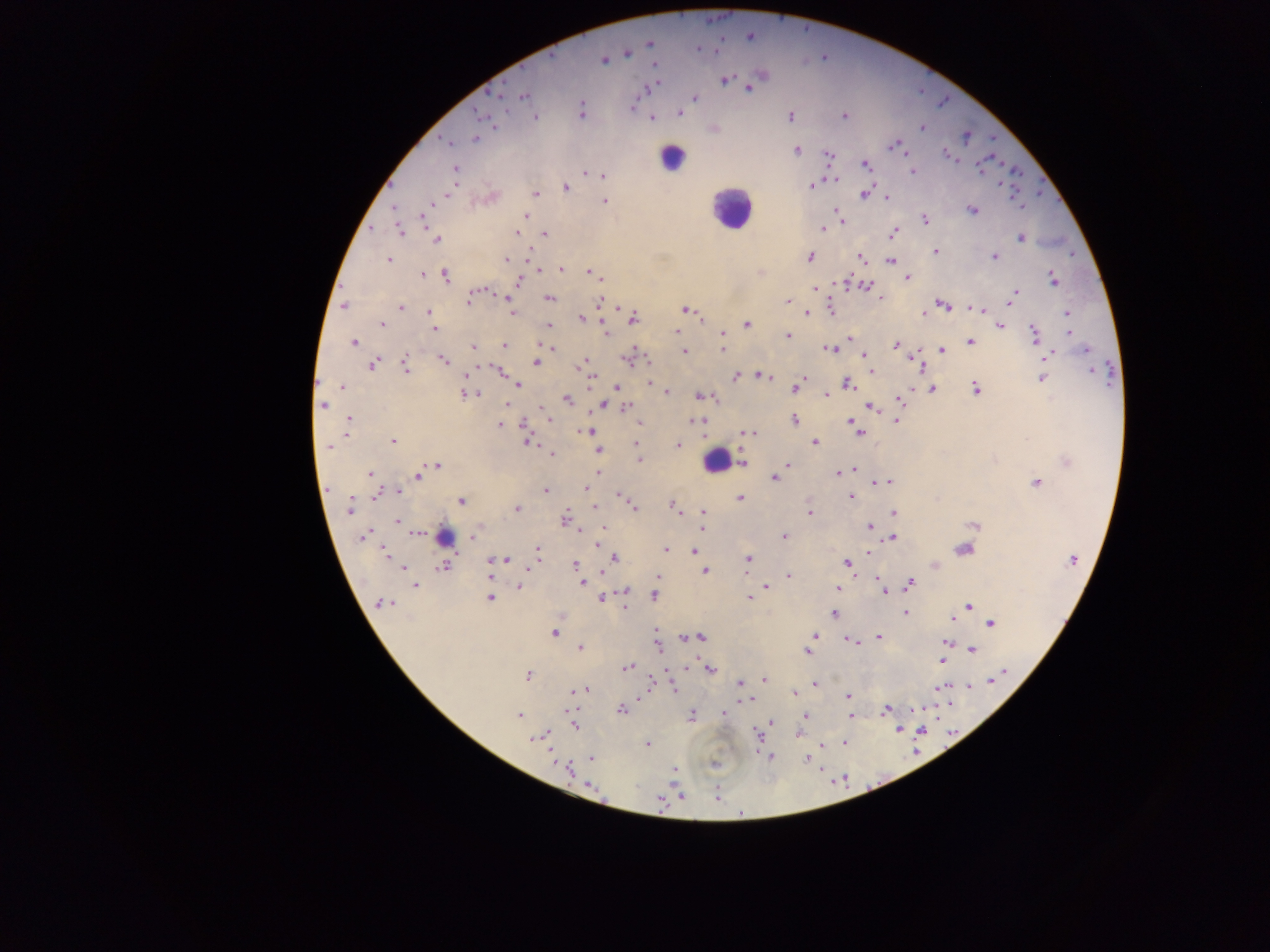

Approximate centers as (x, y) in pixels. Plasmodium parasite locations: (731, 15), (782, 16), (708, 19), (718, 19), (807, 28), (583, 35), (749, 37), (649, 42), (557, 44), (697, 49), (716, 49), (626, 53), (551, 55), (822, 57), (603, 59), (654, 65), (521, 66), (928, 70), (724, 80), (504, 84), (650, 86), (748, 86), (485, 90), (922, 93), (500, 95), (522, 96), (694, 98), (947, 100), (939, 105), (631, 107), (580, 112), (479, 113), (678, 113), (844, 115), (535, 116), (790, 116), (651, 118), (494, 127), (922, 127), (713, 129), (966, 136), (476, 138), (992, 139), (445, 141), (896, 144), (796, 149), (902, 151), (945, 153), (829, 155), (992, 157), (956, 162), (1004, 163), (865, 164), (826, 166), (981, 166), (455, 169), (912, 171), (584, 172), (1022, 174), (602, 175), (834, 179), (1042, 180), (998, 184), (812, 185), (389, 186), (875, 186), (565, 188), (449, 191), (535, 193), (865, 193), (1039, 193), (490, 196), (887, 197), (1059, 199), (605, 200), (1017, 202), (431, 203), (1020, 206), (394, 208), (972, 210), (836, 211), (526, 216), (840, 216), (424, 219), (924, 220), (842, 221), (371, 228), (821, 228), (398, 231), (893, 232), (517, 234), (543, 234), (1020, 237), (437, 239), (935, 251), (527, 254), (1071, 255), (995, 256), (810, 257), (860, 258), (388, 259), (505, 259), (891, 260), (560, 268), (541, 270), (759, 272), (852, 273), (441, 274), (592, 274), (423, 275), (444, 275), (599, 277), (907, 278), (1053, 279), (518, 281), (842, 283), (340, 284), (864, 285), (813, 288), (481, 289), (476, 293), (1014, 293), (504, 296), (549, 297), (882, 298), (468, 299), (1010, 299), (787, 301), (599, 302), (943, 304), (344, 305), (617, 306), (401, 307), (829, 307), (975, 308), (686, 309), (981, 309), (429, 311), (511, 312), (924, 312), (806, 313), (1067, 313), (581, 318), (703, 318), (632, 319), (381, 324), (746, 324), (548, 326), (999, 326), (601, 327), (433, 328), (677, 331), (1069, 331), (606, 332), (722, 333), (1034, 335), (788, 336), (850, 338), (353, 342), (969, 342), (540, 344), (503, 345), (895, 345), (472, 346), (550, 346), (721, 348), (828, 348), (942, 350), (1085, 350), (683, 352), (863, 353), (1048, 355), (627, 359), (915, 359), (647, 360), (444, 361), (535, 362), (372, 364), (489, 364), (1110, 364), (405, 365), (580, 365), (476, 366), (1094, 369), (870, 370), (501, 371), (467, 376), (734, 376), (760, 376), (766, 376), (590, 378), (1041, 378), (317, 382), (848, 382), (648, 383), (1110, 383), (518, 384), (342, 386), (616, 387), (795, 387), (975, 388), (933, 389), (667, 392), (467, 393), (474, 393), (827, 394), (700, 395), (716, 398), (899, 398), (566, 399), (506, 404), (322, 405), (602, 405), (625, 407), (542, 408), (870, 408), (543, 413), (547, 415), (589, 415), (349, 418), (549, 419), (896, 420), (695, 421), (794, 421), (639, 422), (851, 422), (499, 424), (523, 425), (347, 426), (856, 428), (588, 431), (345, 433), (743, 433), (752, 433), (860, 434), (1027, 438), (391, 441), (527, 441), (636, 442), (814, 442), (537, 444), (678, 445), (328, 448), (597, 450), (638, 452), (551, 454), (639, 459), (1067, 462), (743, 463), (788, 464), (437, 465), (853, 470), (597, 472), (837, 472), (370, 473), (417, 475), (774, 478), (887, 482), (876, 483), (1036, 483), (585, 488), (328, 489), (398, 490), (544, 490), (378, 493), (616, 495), (851, 496), (623, 498), (742, 498), (461, 501), (673, 505), (632, 506), (349, 507), (594, 507), (517, 508), (702, 512), (893, 512), (810, 513), (564, 519), (398, 520), (973, 525), (869, 526), (603, 527), (703, 527), (581, 530), (415, 533), (474, 533), (363, 535), (783, 536), (892, 536), (882, 540), (599, 543), (964, 549), (665, 550), (537, 551), (695, 551), (868, 551), (383, 553), (614, 558), (502, 559), (747, 559), (1073, 559), (489, 560), (846, 563), (443, 565), (574, 565), (934, 565), (401, 567), (659, 570), (705, 570), (489, 572), (600, 573), (857, 574), (746, 575), (788, 575), (657, 576), (877, 576), (581, 582), (415, 584), (908, 584), (519, 586), (766, 587), (880, 587), (836, 588), (624, 591), (884, 591), (655, 595), (489, 597), (599, 597), (748, 598), (383, 603), (968, 605), (966, 606), (624, 607), (834, 613), (905, 613), (952, 618), (989, 622), (655, 630), (553, 633), (700, 636), (814, 636), (685, 637), (879, 637), (848, 639), (946, 643), (860, 644), (657, 647), (580, 648), (972, 649), (806, 652), (941, 661), (627, 666), (686, 668), (710, 668), (1004, 669), (665, 672), (527, 675), (650, 676), (765, 679), (992, 679), (740, 683), (814, 684), (655, 685), (950, 685), (938, 686), (967, 686), (673, 687), (584, 690), (574, 691), (793, 693), (642, 696), (847, 697), (747, 700), (937, 704), (950, 704), (578, 708), (621, 709), (885, 709), (924, 709), (566, 711), (723, 712), (912, 712), (518, 715), (691, 715), (851, 716), (804, 717), (937, 719), (771, 721), (574, 726), (899, 728), (920, 731), (952, 731), (797, 733), (757, 734), (544, 735), (537, 737), (913, 740), (844, 741), (647, 744), (823, 744), (947, 748), (916, 750), (756, 751), (590, 757), (771, 757), (806, 758), (553, 760), (713, 764), (674, 768), (568, 769), (823, 769), (844, 775), (881, 782), (834, 783), (672, 784), (589, 786), (868, 786), (718, 787), (847, 787), (685, 796), (719, 796), (661, 798), (605, 801), (660, 811), (741, 814). Leukocyte locations: (671, 157), (731, 208), (716, 461), (443, 536). Thick blood smear. One field of view. Photographed through a microscope with a mobile-phone camera. Image is 1270×952 pixels. Sample from Ghana.